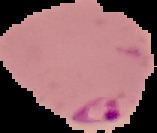

Summary:
  - Image type: segmented cell region on a black background
  - Malaria status: parasitized
  - Preparation: thin blood smear
  - Image size: 157×133 pixels